Name the parasite shown.
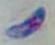

This is Toxoplasma gondii.

modality = photomicrograph
magnification = 1000x